Locate and identify every blood parasite.
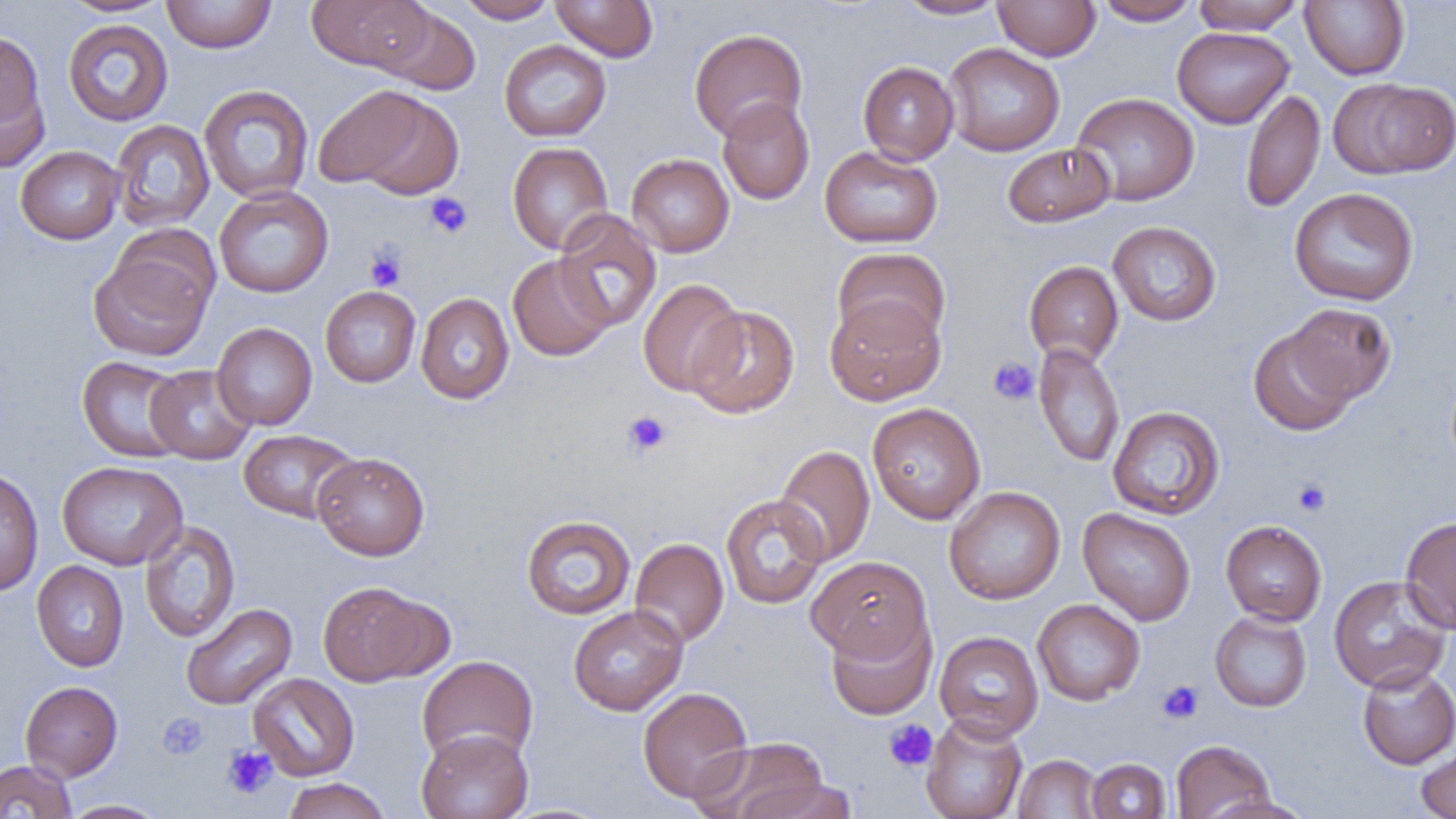
No blood parasites observed.

Approximate bounding boxes as [x1, y1, x2, y2] in pixels. Uninfected red blood cell locations: [57, 0, 174, 17], [161, 0, 276, 53], [307, 0, 431, 73], [456, 0, 558, 23], [550, 0, 659, 62], [894, 0, 1009, 20], [1093, 0, 1201, 26], [1191, 0, 1304, 34], [1300, 0, 1410, 80], [993, 1, 1101, 61], [375, 4, 481, 96], [63, 19, 174, 126], [1172, 26, 1294, 129], [689, 28, 808, 141], [0, 30, 51, 169], [499, 40, 611, 142], [943, 43, 1065, 156], [858, 61, 959, 165], [1328, 77, 1456, 180], [199, 84, 314, 203], [311, 85, 436, 192], [1241, 89, 1326, 213], [1071, 92, 1200, 206], [717, 97, 815, 205], [110, 119, 215, 232], [507, 142, 613, 255], [1003, 143, 1115, 227], [15, 145, 124, 245], [819, 145, 943, 248], [626, 153, 734, 257], [213, 186, 334, 298], [1289, 188, 1419, 306], [553, 210, 662, 332], [1108, 221, 1222, 326], [88, 245, 215, 362], [833, 247, 950, 347], [507, 254, 614, 361], [1024, 261, 1124, 366], [638, 279, 746, 396], [320, 286, 421, 387], [415, 292, 514, 405], [825, 294, 944, 405], [1285, 303, 1397, 405], [686, 305, 800, 418], [212, 322, 317, 430], [1248, 325, 1358, 436], [1033, 343, 1125, 468], [77, 356, 190, 462], [145, 364, 256, 465], [867, 402, 986, 524], [1108, 406, 1225, 520], [238, 429, 359, 523], [774, 444, 875, 566], [312, 452, 430, 560], [57, 460, 188, 570], [0, 467, 43, 596], [944, 486, 1066, 605], [720, 494, 829, 609], [1078, 507, 1196, 625], [521, 515, 635, 620], [1400, 515, 1456, 634], [1220, 520, 1327, 625], [139, 521, 240, 643], [629, 537, 729, 648], [806, 555, 932, 663], [31, 560, 129, 672], [1328, 575, 1452, 693], [318, 581, 435, 686], [1032, 599, 1145, 705], [181, 603, 297, 711], [568, 604, 688, 716], [1209, 610, 1312, 712], [825, 611, 937, 720], [934, 631, 1044, 740], [416, 655, 538, 767], [1357, 665, 1456, 769], [247, 672, 360, 781], [20, 680, 122, 781], [637, 686, 753, 804], [920, 714, 1028, 819], [416, 727, 534, 819], [694, 736, 831, 819], [1171, 739, 1275, 819], [1416, 742, 1456, 818], [1013, 754, 1103, 818], [1086, 758, 1171, 818], [0, 760, 77, 818], [739, 776, 858, 819], [282, 778, 392, 819], [1203, 795, 1314, 819], [60, 799, 168, 819]. Platelet locations: [424, 192, 473, 239], [365, 247, 406, 291], [988, 356, 1040, 406], [622, 410, 672, 458], [1293, 479, 1330, 516], [1157, 679, 1204, 724], [157, 712, 209, 760], [884, 720, 938, 771], [222, 745, 277, 798]. Slide-level diagnosis: negative for blood parasites. Thin blood smear. 1000x magnification. Light microscopy. One field of a larger specimen. Image is 1456×819 pixels.